Name the parasite shown.
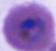
Plasmodium.

400x or 1000x magnification. Photomicrograph.